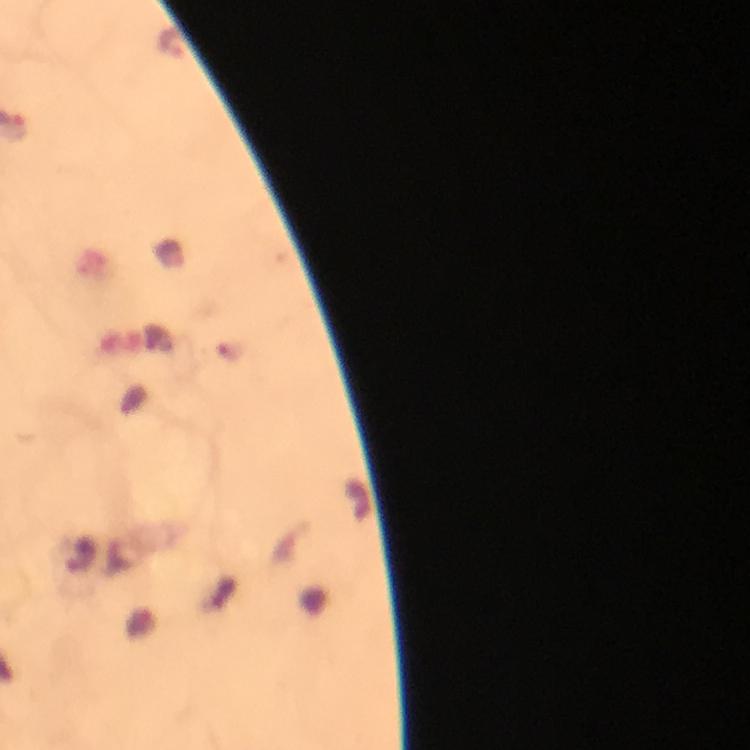 Approximate centers as [x, y] in pixels. Malaria parasite locations: [170, 42]. Cropped region of a single field of view. From a malaria diagnostic workup. Image is 750×750 pixels. 100x magnification. Giemsa stain. Photographed with a smartphone mounted on the microscope. Thick blood film. Immersion oil applied.